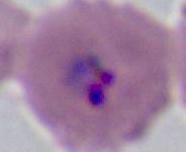
A Plasmodium parasite is seen. Captured at either 400x or 1000x magnification. Photomicrograph.